Name the blood parasite species.
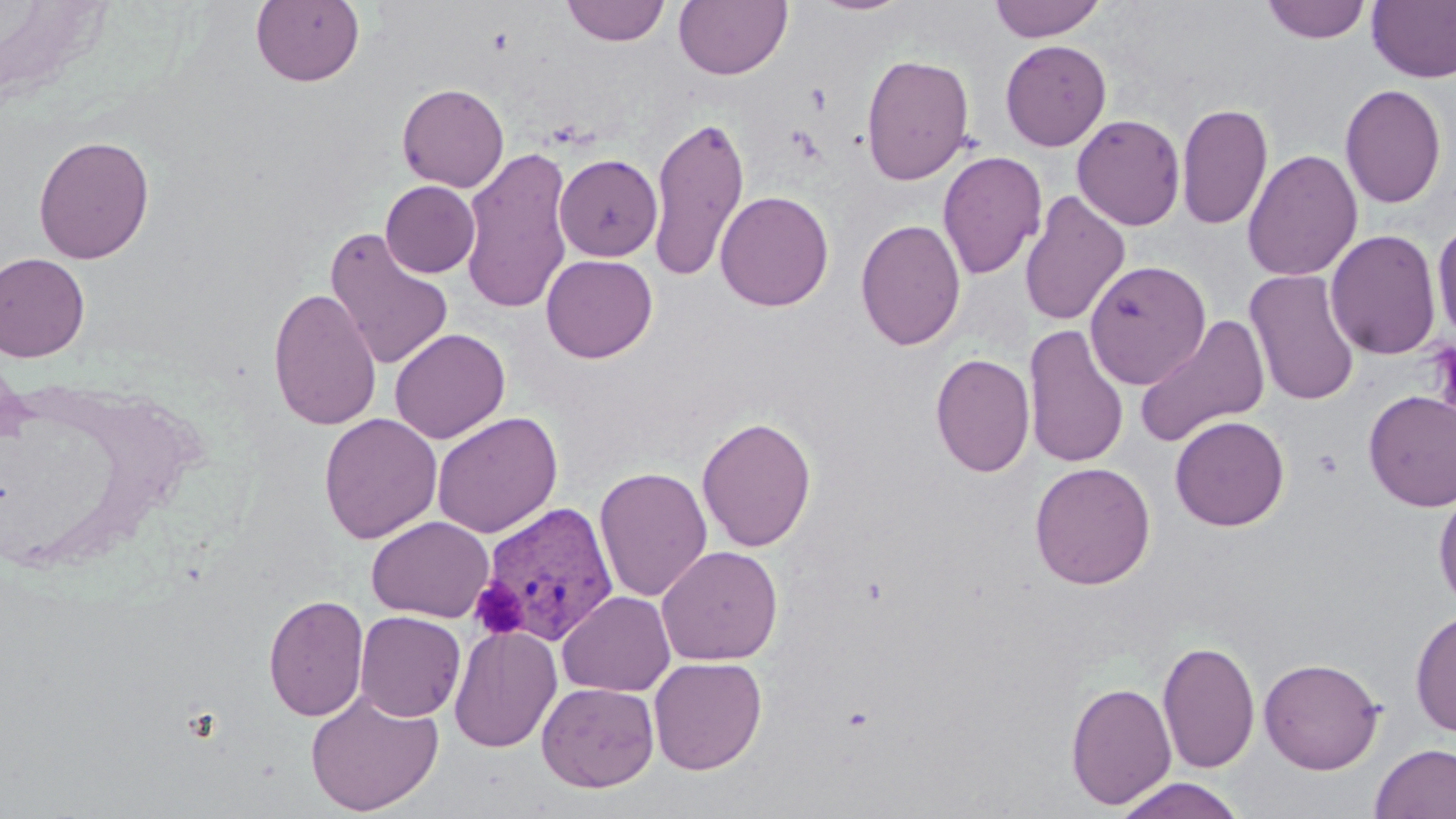
Plasmodium vivax.

Summary:
  - Coordinate format: approximate bounding boxes as [x1, y1, x2, y2] in pixels
  - Uninfected red blood cell locations: [250, 0, 365, 87], [561, 0, 670, 46], [673, 0, 792, 80], [809, 0, 915, 16], [989, 0, 1107, 42], [1261, 1, 1371, 44], [1367, 1, 1456, 83], [1000, 39, 1112, 151], [860, 52, 975, 185], [397, 82, 509, 192], [1339, 83, 1447, 209], [1176, 101, 1273, 230], [649, 113, 750, 283], [1071, 113, 1186, 230], [33, 134, 155, 264], [460, 147, 575, 315], [1242, 149, 1363, 282], [936, 150, 1047, 280], [555, 154, 662, 261], [380, 180, 480, 278], [715, 190, 834, 312], [1019, 190, 1130, 327], [855, 218, 966, 351], [1432, 218, 1456, 345], [324, 228, 454, 371], [1326, 228, 1442, 361], [0, 252, 89, 362], [541, 254, 658, 363], [1084, 260, 1210, 389], [1244, 269, 1361, 406], [268, 287, 382, 431], [1134, 313, 1271, 449], [1024, 323, 1129, 469], [390, 329, 510, 443], [930, 353, 1035, 478], [1363, 390, 1456, 511], [432, 411, 563, 538], [319, 413, 442, 544], [696, 415, 817, 552], [1170, 415, 1289, 531], [1029, 461, 1156, 590], [594, 466, 713, 602], [1433, 484, 1456, 610], [366, 515, 494, 622], [657, 545, 783, 665], [557, 590, 676, 696], [263, 593, 369, 721], [1410, 609, 1456, 738], [355, 611, 466, 721], [449, 624, 562, 752], [1157, 639, 1260, 774], [648, 656, 767, 774], [1258, 657, 1384, 774], [537, 681, 660, 792], [1065, 681, 1177, 810], [305, 689, 444, 816], [1369, 743, 1456, 819], [1113, 776, 1247, 819]
  - Platelet locations: [470, 579, 528, 638]
  - Plasmodium vivax-infected red blood cell locations: [475, 501, 622, 646]
  - Field of view: one of a larger specimen
  - Modality: light microscopy
  - Magnification: 1000x
  - Preparation: thin blood film
  - Image size: 1456×819 pixels
  - Stain: May-Grünwald-Giemsa